Locate every Plasmodium falciparum-infected red blood cell.
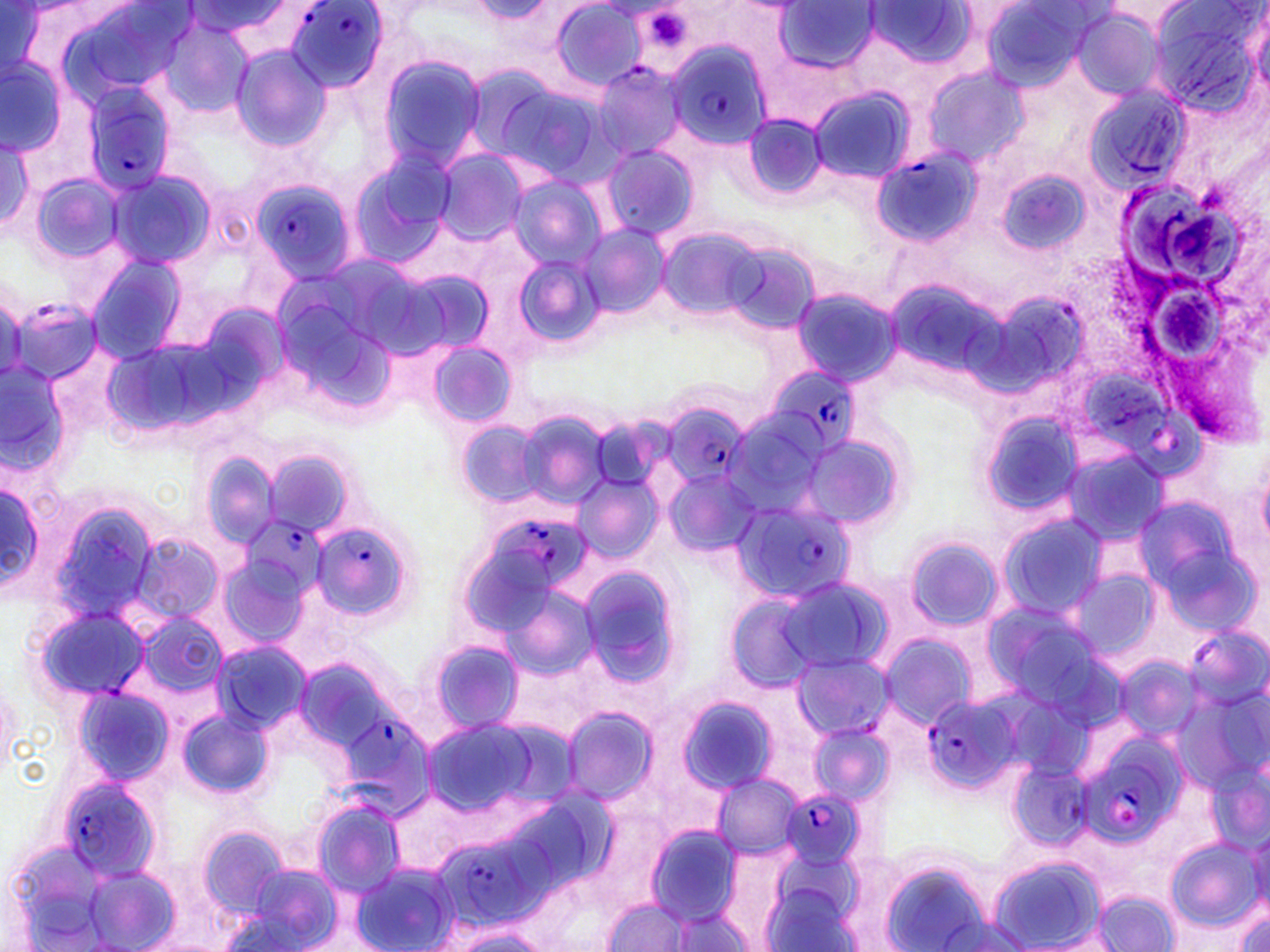
Approximate bounding boxes as (x1, y1, x2, y2) in pixels.
Plasmodium falciparum-infected red blood cells (subset): (287, 1, 386, 92), (665, 40, 770, 148), (591, 62, 686, 161), (81, 82, 178, 198), (869, 147, 979, 249), (251, 180, 354, 282), (764, 368, 862, 456), (665, 406, 753, 489), (728, 498, 857, 604), (488, 516, 590, 590), (243, 518, 329, 600), (308, 520, 415, 628), (924, 690, 1023, 793), (344, 717, 443, 821), (1084, 736, 1186, 841), (55, 777, 164, 882), (780, 788, 864, 869), (463, 838, 566, 935).

Summary:
  - Platelet locations: (648, 12, 693, 49)
  - Uninfected red blood cell locations (subset): (548, 0, 646, 91), (866, 0, 977, 70), (975, 0, 1099, 94), (1146, 0, 1266, 117), (773, 1, 879, 75), (470, 2, 551, 22), (186, 3, 294, 40), (1071, 9, 1163, 97), (158, 18, 256, 121), (231, 47, 330, 153), (377, 54, 486, 172), (0, 56, 64, 154), (460, 61, 561, 162), (923, 66, 1025, 168), (495, 80, 617, 185), (1086, 84, 1192, 192), (808, 87, 913, 183), (738, 114, 828, 202), (0, 136, 35, 228), (600, 146, 698, 240), (431, 149, 526, 245), (346, 152, 455, 271), (995, 169, 1094, 257), (105, 170, 216, 271), (28, 174, 124, 266), (509, 176, 604, 272), (579, 222, 669, 321), (655, 226, 765, 320), (721, 241, 820, 334), (87, 252, 185, 363), (517, 253, 602, 346), (389, 264, 499, 361), (884, 274, 1012, 390), (791, 287, 900, 387), (977, 287, 1090, 398), (427, 341, 516, 429), (1, 361, 68, 476), (513, 409, 611, 509), (976, 409, 1086, 523), (722, 412, 829, 517), (455, 419, 546, 509), (797, 435, 906, 531), (1062, 445, 1170, 550), (259, 448, 358, 538), (201, 452, 281, 546), (1255, 452, 1270, 547), (661, 466, 761, 560), (571, 476, 663, 563), (0, 479, 45, 598), (44, 497, 162, 625), (997, 513, 1110, 619), (132, 533, 223, 623), (903, 536, 1003, 631), (575, 563, 686, 689), (1065, 567, 1163, 667), (775, 575, 892, 677), (494, 580, 605, 686), (723, 592, 823, 694), (30, 603, 152, 707), (136, 612, 225, 701), (878, 633, 978, 727), (424, 638, 525, 735), (212, 640, 311, 734), (789, 653, 891, 740), (1114, 653, 1203, 743), (69, 684, 175, 786), (673, 693, 783, 798), (562, 705, 659, 802), (174, 708, 275, 800), (419, 716, 546, 813), (808, 724, 893, 808), (1009, 760, 1093, 849), (711, 773, 802, 856), (387, 788, 478, 876), (310, 797, 408, 897), (196, 823, 292, 919), (643, 824, 744, 925), (1163, 835, 1262, 933), (2, 839, 123, 949), (988, 854, 1109, 952), (877, 859, 994, 952), (350, 863, 457, 952), (235, 864, 345, 952), (84, 866, 180, 951), (1093, 891, 1180, 950), (597, 896, 692, 949), (1234, 904, 1269, 952), (663, 907, 756, 952), (931, 915, 1035, 951), (447, 926, 553, 951)
  - Slide-level diagnosis: Plasmodium falciparum
  - Modality: optical microscopy
  - Field of view: one of a larger specimen
  - Magnification: 1000x
  - Stain: May-Grünwald-Giemsa
  - Preparation: thin blood film
  - Image size: 1270×952 pixels